Assess the morphology of the erythrocytes.
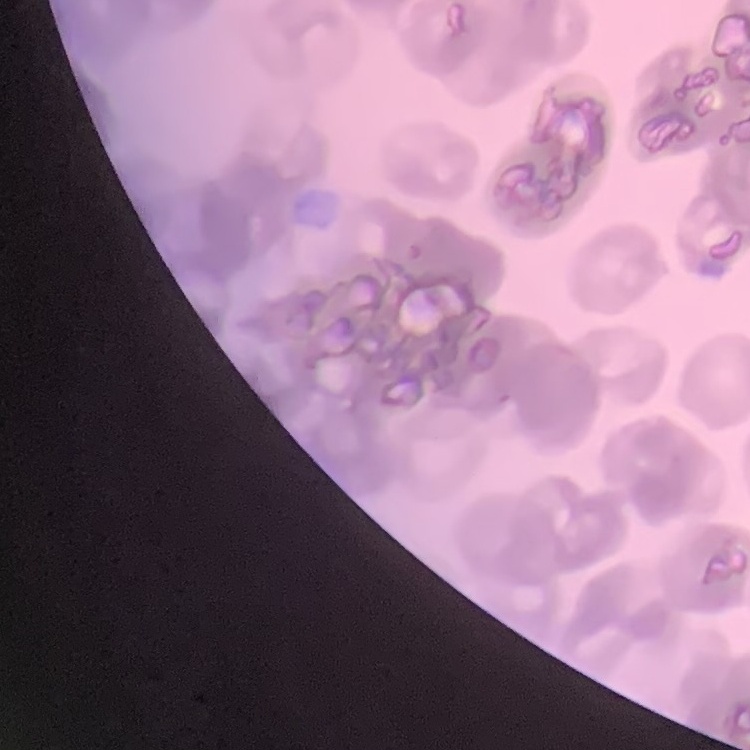

Rouleaux formation.

{
  "preparation": "thin blood film",
  "image_type": "one tile cut from a larger photomicrograph",
  "stain": "Field's or Giemsa"
}